Name the cell type shown.
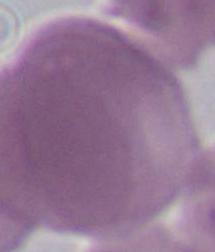
An erythrocyte.

{
  "magnification": "1000x",
  "modality": "photomicrograph"
}